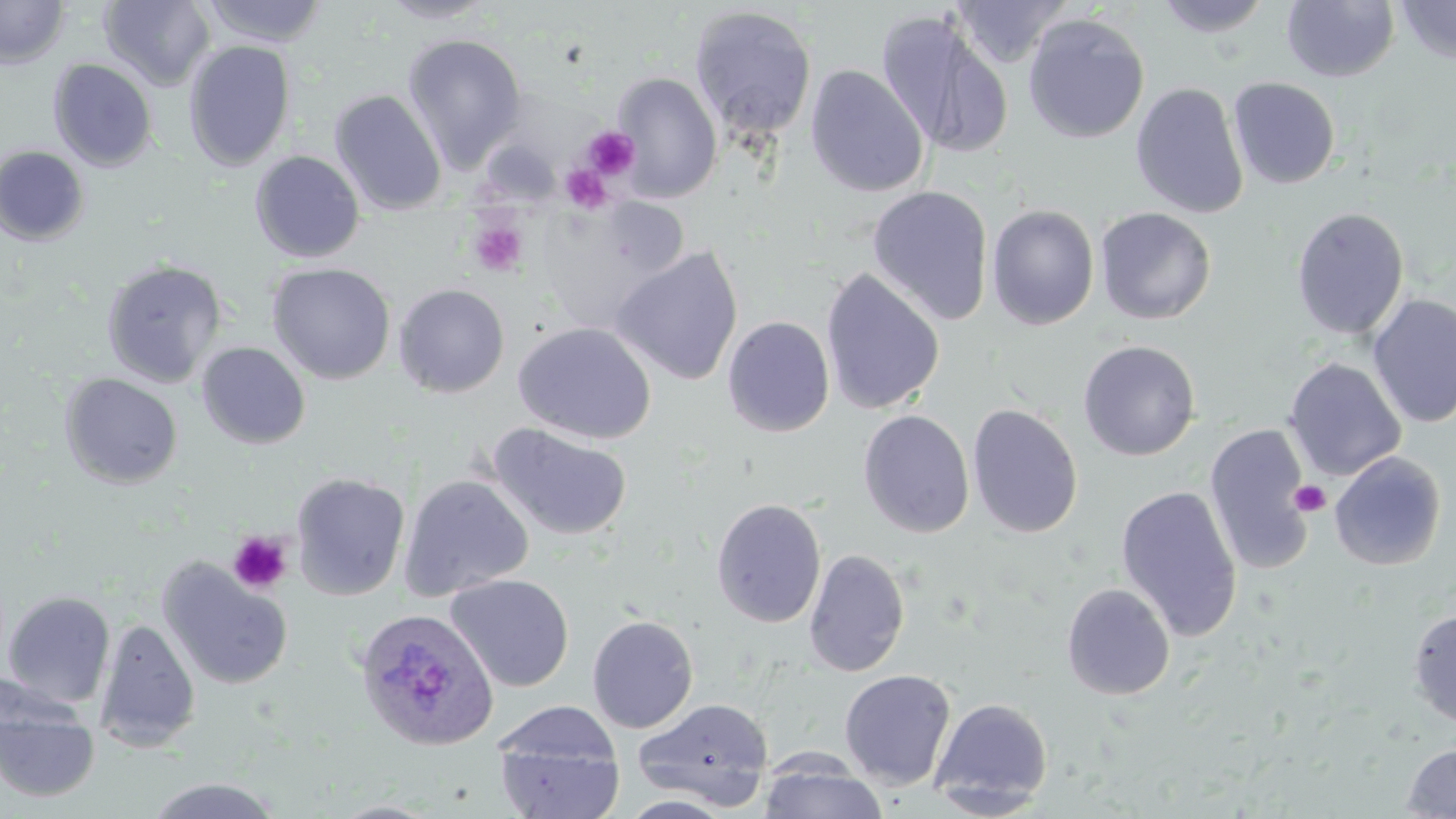

Approximate bounding boxes as named x1/y1/x2/y2 corners in pixels. Platelet locations: (x1=582, y1=127, x2=640, y2=180), (x1=558, y1=164, x2=612, y2=213), (x1=467, y1=217, x2=529, y2=277), (x1=1289, y1=479, x2=1331, y2=516), (x1=227, y1=530, x2=292, y2=595). Plasmodium ovale-infected red blood cell locations: (x1=354, y1=607, x2=499, y2=751). Uninfected red blood cell locations: (x1=99, y1=0, x2=216, y2=90), (x1=201, y1=0, x2=329, y2=48), (x1=379, y1=0, x2=497, y2=24), (x1=949, y1=0, x2=1071, y2=68), (x1=1153, y1=0, x2=1275, y2=37), (x1=1394, y1=0, x2=1456, y2=65), (x1=0, y1=1, x2=69, y2=69), (x1=1282, y1=1, x2=1399, y2=82), (x1=689, y1=6, x2=817, y2=143), (x1=876, y1=10, x2=1014, y2=158), (x1=1023, y1=13, x2=1149, y2=144), (x1=402, y1=34, x2=527, y2=171), (x1=183, y1=41, x2=296, y2=171), (x1=48, y1=58, x2=157, y2=171), (x1=805, y1=64, x2=928, y2=198), (x1=609, y1=71, x2=724, y2=202), (x1=1228, y1=77, x2=1341, y2=189), (x1=1130, y1=82, x2=1249, y2=218), (x1=330, y1=89, x2=447, y2=215), (x1=0, y1=145, x2=89, y2=245), (x1=250, y1=150, x2=365, y2=263), (x1=866, y1=185, x2=994, y2=326), (x1=533, y1=198, x2=689, y2=333), (x1=986, y1=204, x2=1100, y2=330), (x1=1291, y1=206, x2=1410, y2=340), (x1=1094, y1=207, x2=1216, y2=325), (x1=611, y1=245, x2=744, y2=386), (x1=101, y1=259, x2=226, y2=388), (x1=267, y1=263, x2=396, y2=385), (x1=820, y1=267, x2=945, y2=415), (x1=393, y1=284, x2=511, y2=397), (x1=1367, y1=293, x2=1456, y2=428), (x1=722, y1=316, x2=836, y2=437), (x1=514, y1=321, x2=657, y2=444), (x1=1078, y1=340, x2=1201, y2=461), (x1=196, y1=341, x2=311, y2=449), (x1=1284, y1=358, x2=1407, y2=481), (x1=60, y1=373, x2=184, y2=489), (x1=967, y1=403, x2=1084, y2=539), (x1=858, y1=410, x2=975, y2=538), (x1=487, y1=422, x2=632, y2=542), (x1=1204, y1=424, x2=1315, y2=575), (x1=1329, y1=452, x2=1446, y2=571), (x1=290, y1=472, x2=410, y2=601), (x1=398, y1=474, x2=534, y2=601), (x1=1115, y1=484, x2=1243, y2=642), (x1=711, y1=497, x2=827, y2=628), (x1=803, y1=548, x2=911, y2=677), (x1=157, y1=559, x2=293, y2=690), (x1=446, y1=574, x2=574, y2=692), (x1=1061, y1=582, x2=1175, y2=701), (x1=2, y1=591, x2=115, y2=709), (x1=1407, y1=609, x2=1456, y2=728), (x1=587, y1=614, x2=699, y2=733), (x1=94, y1=618, x2=201, y2=753), (x1=839, y1=669, x2=956, y2=790), (x1=0, y1=692, x2=99, y2=802), (x1=633, y1=696, x2=774, y2=809), (x1=929, y1=697, x2=1054, y2=810), (x1=493, y1=701, x2=622, y2=778), (x1=494, y1=732, x2=625, y2=819), (x1=1401, y1=744, x2=1456, y2=818), (x1=757, y1=760, x2=888, y2=818), (x1=144, y1=777, x2=284, y2=818), (x1=616, y1=795, x2=736, y2=818). Slide-level diagnosis: Plasmodium ovale. Thin blood smear. Single field of view. Optical microscopy. 1000x magnification. May-Grünwald-Giemsa-stained preparation. Image is 1456×819 pixels.